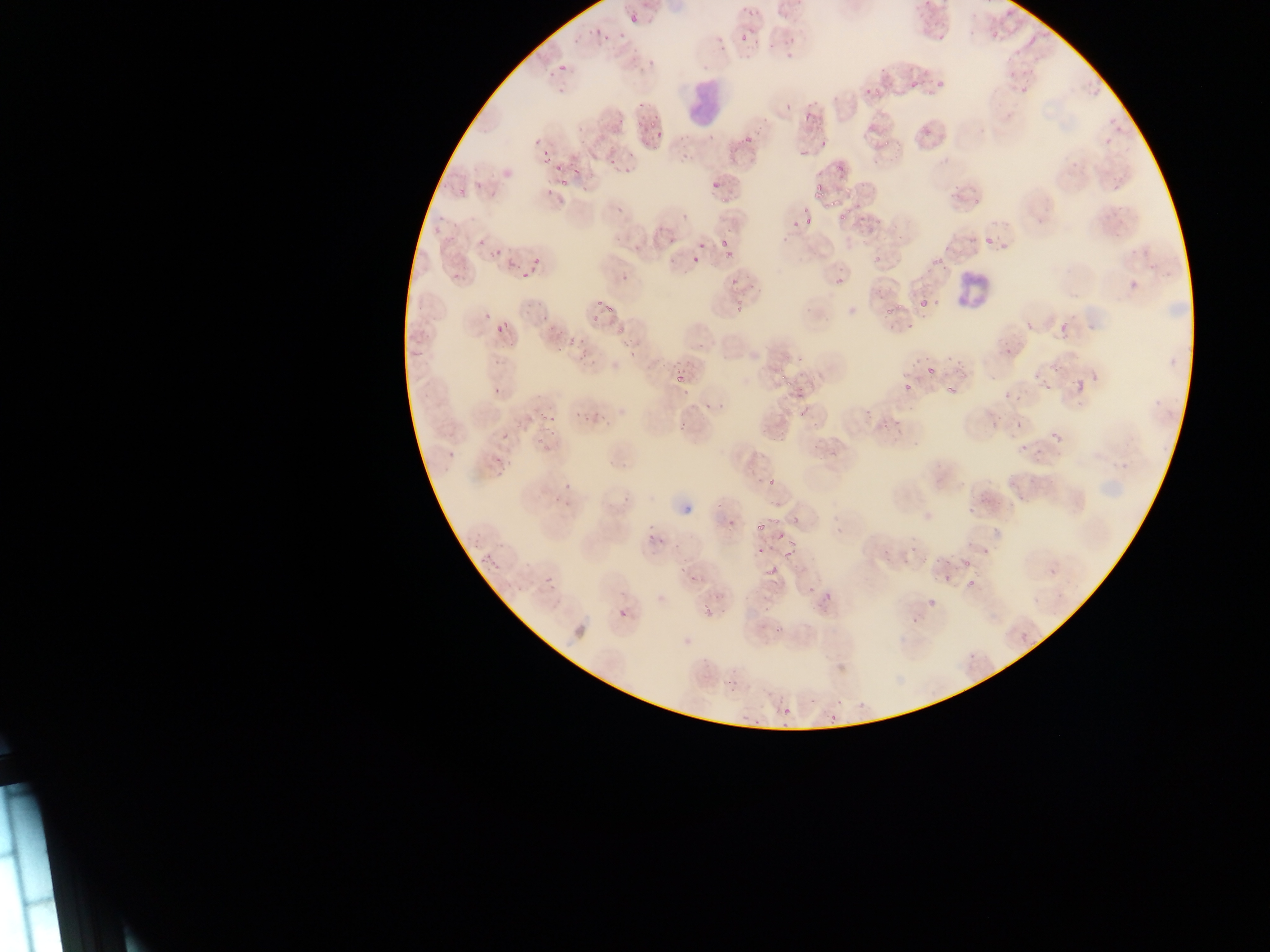
Approximate bounding boxes as {left, top, right, bottom} in pixels.
Summary:
  - Malaria parasite locations: {626, 11, 637, 26}, {749, 13, 768, 29}, {777, 15, 813, 68}, {588, 20, 611, 38}, {739, 34, 748, 43}, {1029, 36, 1037, 45}, {558, 63, 569, 73}, {915, 75, 946, 87}, {911, 82, 919, 89}, {777, 98, 797, 116}, {586, 102, 620, 137}, {800, 105, 824, 134}, {631, 114, 645, 128}, {644, 124, 670, 145}, {741, 132, 756, 147}, {796, 146, 813, 164}, {605, 152, 623, 164}, {540, 153, 553, 166}, {539, 161, 576, 190}, {808, 179, 833, 200}, {714, 189, 743, 207}, {834, 204, 860, 221}, {801, 214, 811, 226}, {786, 222, 797, 232}, {715, 231, 741, 252}, {984, 237, 992, 244}, {515, 244, 551, 277}, {497, 251, 516, 269}, {612, 252, 638, 280}, {691, 254, 700, 263}, {832, 264, 850, 293}, {725, 270, 744, 285}, {729, 288, 755, 319}, {587, 289, 612, 310}, {917, 289, 942, 315}, {887, 302, 904, 315}, {589, 304, 609, 325}, {1060, 306, 1085, 342}, {493, 322, 506, 334}, {547, 330, 573, 352}, {920, 356, 954, 387}, {672, 365, 698, 385}, {1032, 370, 1049, 383}, {777, 373, 790, 385}, {487, 375, 510, 399}, {942, 378, 967, 399}, {892, 379, 913, 407}, {1075, 380, 1088, 393}, {786, 382, 801, 400}, {1015, 395, 1025, 404}, {538, 402, 563, 428}, {871, 408, 883, 426}, {797, 411, 807, 423}, {1013, 420, 1020, 429}, {894, 421, 905, 437}, {805, 430, 818, 451}, {1044, 432, 1059, 441}, {1008, 437, 1027, 454}, {824, 450, 838, 462}, {1006, 463, 1037, 494}, {768, 477, 776, 486}, {760, 506, 780, 528}, {774, 524, 787, 548}, {640, 525, 669, 544}, {685, 533, 694, 547}, {753, 540, 765, 552}, {908, 544, 932, 565}, {776, 546, 788, 558}, {483, 553, 493, 564}, {940, 559, 967, 581}, {676, 566, 687, 578}, {964, 567, 993, 593}, {1048, 569, 1057, 578}, {543, 574, 554, 586}, {617, 607, 626, 619}, {701, 608, 708, 618}, {1020, 632, 1029, 641}, {724, 683, 731, 694}, {769, 703, 794, 716}
  - Leukocyte locations: {681, 80, 727, 127}, {944, 266, 1003, 307}
  - Country: Ghana
  - Image size: 1270×952 pixels
  - Capture: mobile-phone photograph through a microscope
  - Field of view: single
  - Preparation: thin blood smear